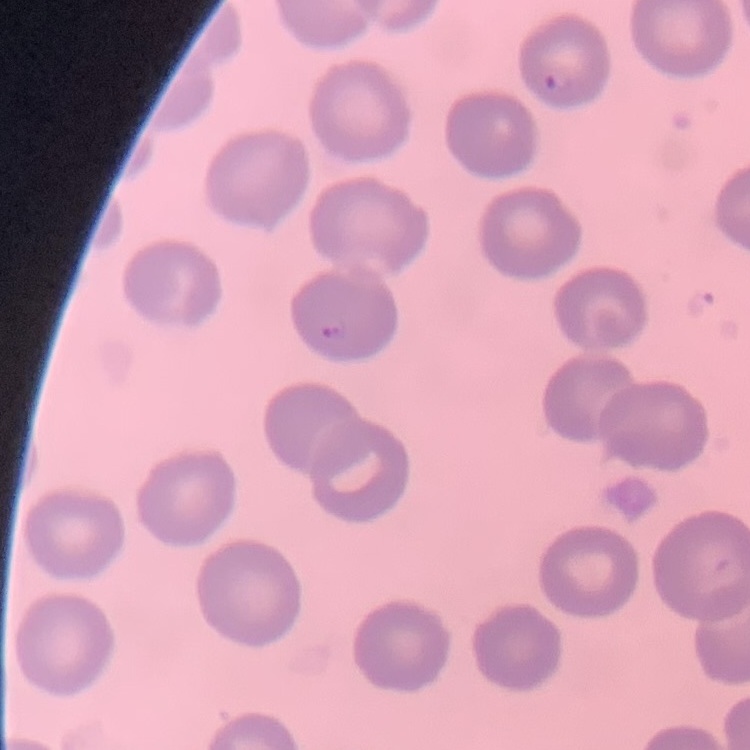

Summary:
  - Red blood cell morphology: no rouleaux formation
  - Stain: Field's or Giemsa
  - Image type: one tile cut from a larger photomicrograph
  - Preparation: thin blood smear